Describe the morphology of the red blood cells.
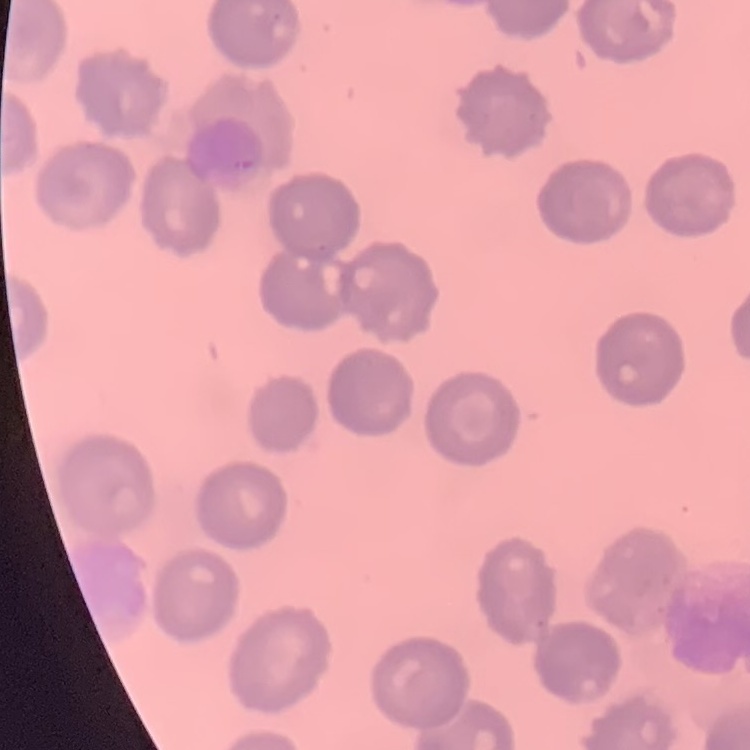
No rouleaux formation.

Summary:
  - Preparation: thin blood film
  - Stain: Field's or Giemsa
  - Image type: square crop of a larger photomicrograph